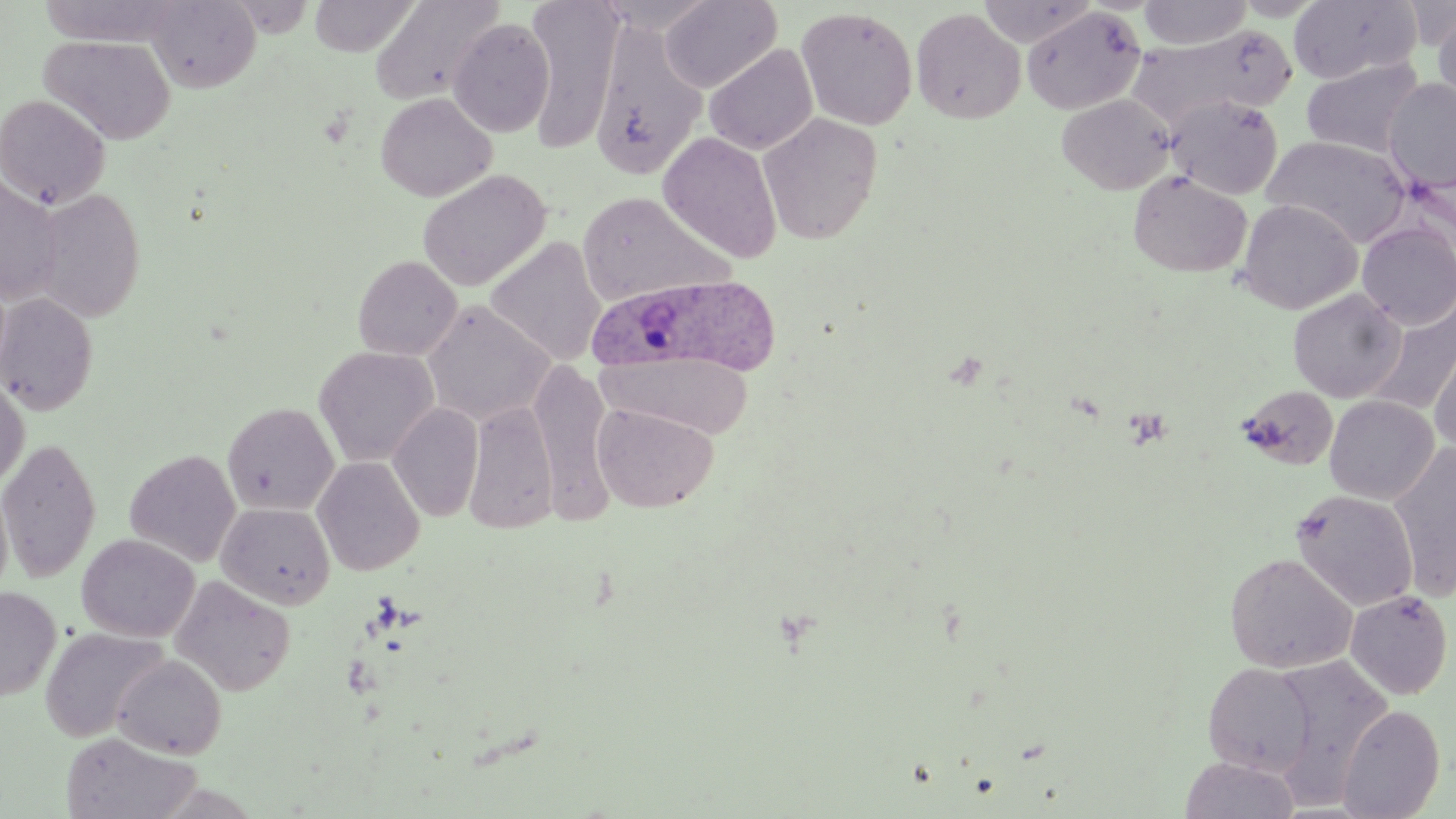

Approximate bounding boxes as [x1, y1, x2, y2] in pixels. Plasmodium ovale-infected red blood cell locations: [589, 274, 784, 375]. Uninfected red blood cell locations: [145, 0, 261, 93], [309, 0, 418, 57], [369, 0, 505, 107], [524, 0, 623, 153], [660, 0, 781, 93], [977, 0, 1099, 47], [1138, 0, 1253, 48], [1233, 0, 1326, 21], [1289, 0, 1419, 85], [224, 1, 316, 37], [1432, 6, 1456, 110], [796, 7, 918, 130], [1021, 7, 1146, 115], [910, 8, 1025, 125], [447, 18, 555, 137], [590, 19, 708, 180], [1129, 24, 1293, 134], [39, 34, 175, 145], [704, 44, 818, 155], [1301, 57, 1424, 159], [1384, 78, 1456, 193], [375, 92, 497, 202], [0, 93, 110, 209], [1056, 94, 1176, 195], [1166, 95, 1284, 200], [758, 113, 883, 244], [658, 133, 783, 263], [1262, 135, 1412, 247], [417, 168, 551, 291], [1128, 170, 1252, 278], [0, 176, 62, 306], [32, 189, 146, 322], [576, 191, 732, 307], [1236, 199, 1362, 314], [1357, 220, 1456, 329], [486, 236, 606, 367], [352, 255, 462, 360], [1287, 289, 1406, 403], [0, 293, 99, 415], [1367, 298, 1456, 416], [421, 301, 555, 426], [1428, 331, 1456, 453], [313, 346, 439, 467], [598, 350, 753, 438], [529, 359, 614, 520], [0, 375, 29, 490], [1237, 385, 1339, 471], [1324, 395, 1438, 504], [463, 400, 559, 534], [222, 402, 339, 516], [592, 402, 718, 513], [388, 403, 484, 522], [0, 437, 101, 583], [1389, 445, 1456, 601], [124, 449, 241, 567], [312, 456, 426, 576], [0, 477, 14, 604], [1291, 489, 1419, 611], [217, 502, 335, 610], [77, 534, 199, 642], [1224, 552, 1357, 672], [170, 576, 296, 696], [0, 587, 60, 700], [1345, 589, 1453, 698], [40, 626, 169, 742], [113, 654, 226, 759], [1266, 654, 1394, 804], [1202, 662, 1317, 776], [1337, 703, 1445, 818], [60, 732, 201, 819], [1179, 756, 1301, 819]. Slide-level diagnosis: Plasmodium ovale. May-Grünwald-Giemsa-stained preparation. Single field of view. Thin blood film. Light microscopy. Image is 1456×819 pixels. 1000x magnification.